Outline each Plasmodium falciparum-infected red blood cell.
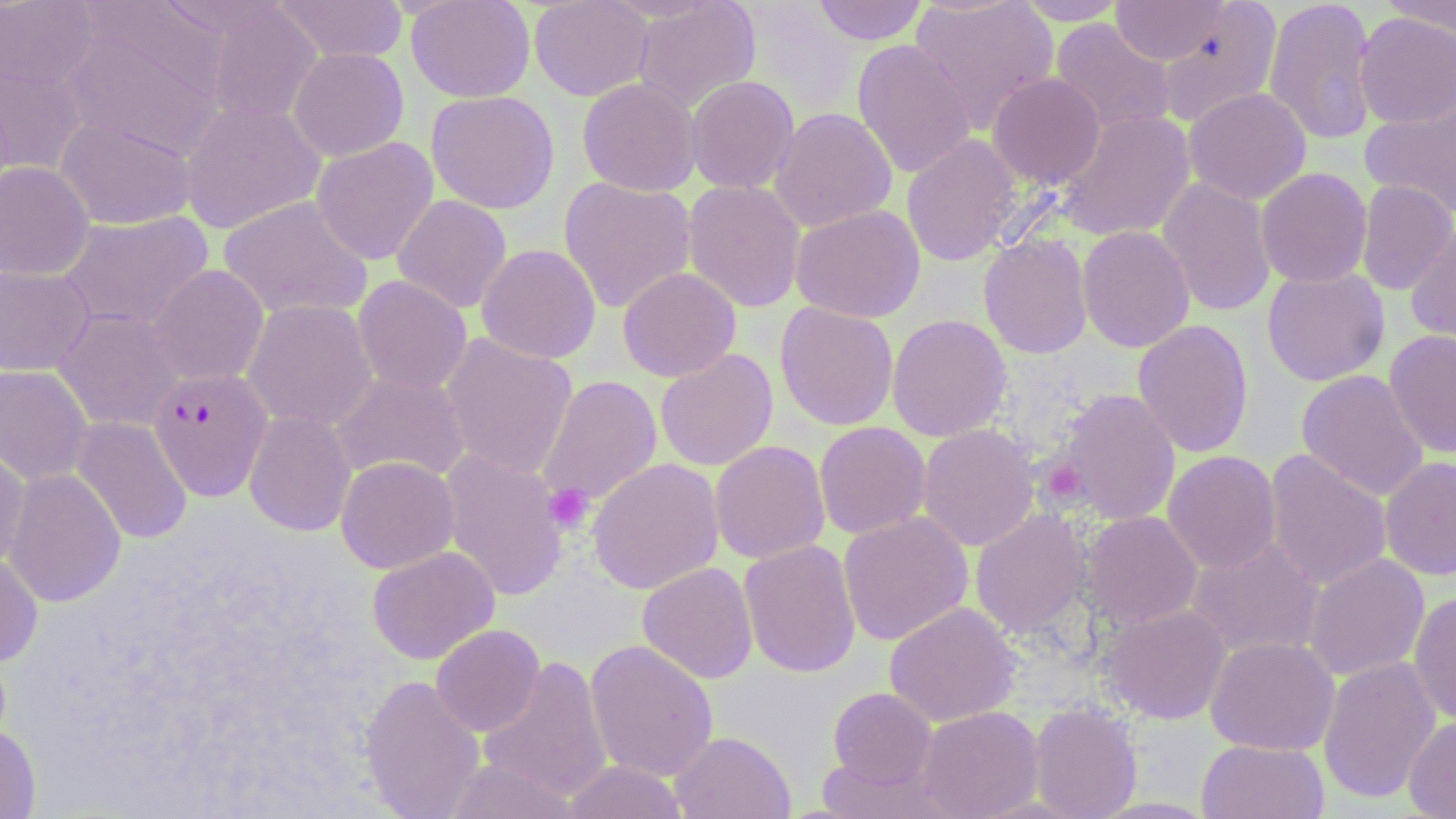
Approximate bounding boxes as (x1, y1, x2, y2) in pixels.
Plasmodium falciparum-infected red blood cells: (149, 367, 272, 501).

Uninfected red blood cell locations: (272, 0, 408, 64), (405, 0, 535, 102), (529, 0, 654, 101), (632, 0, 761, 113), (812, 0, 928, 45), (910, 0, 1058, 130), (1012, 0, 1130, 25), (1111, 0, 1228, 65), (1263, 0, 1378, 145), (0, 1, 98, 89), (1157, 1, 1283, 127), (1382, 1, 1456, 45), (206, 4, 323, 126), (61, 11, 227, 160), (1354, 11, 1456, 128), (1049, 18, 1176, 135), (852, 39, 977, 178), (288, 46, 409, 161), (0, 59, 89, 177), (987, 72, 1105, 189), (686, 76, 799, 195), (577, 77, 702, 197), (1184, 87, 1311, 204), (426, 90, 560, 214), (1360, 97, 1456, 220), (180, 99, 326, 234), (769, 107, 897, 232), (1056, 110, 1196, 241), (55, 115, 196, 230), (901, 133, 1021, 266), (311, 137, 439, 265), (0, 161, 94, 281), (1256, 167, 1373, 288), (558, 176, 697, 313), (1157, 177, 1277, 317), (683, 179, 806, 313), (1355, 180, 1455, 295), (392, 194, 512, 314), (218, 195, 373, 321), (791, 204, 925, 323), (57, 210, 214, 332), (1405, 221, 1456, 351), (1077, 225, 1195, 353), (978, 232, 1093, 360), (476, 243, 601, 364), (0, 264, 95, 376), (148, 264, 269, 386), (617, 267, 742, 382), (1262, 267, 1389, 386), (353, 275, 472, 394), (241, 299, 377, 432), (775, 302, 899, 431), (53, 307, 185, 433), (886, 314, 1013, 441), (1133, 318, 1254, 459), (1384, 329, 1456, 458), (440, 333, 578, 480), (655, 349, 778, 471), (0, 364, 93, 485), (1296, 369, 1429, 502), (330, 371, 470, 484), (537, 375, 662, 506), (1054, 388, 1181, 525), (244, 410, 356, 537), (71, 417, 192, 545), (814, 421, 931, 539), (917, 424, 1040, 551), (709, 440, 830, 564), (0, 444, 31, 569), (438, 448, 569, 601), (1263, 448, 1393, 592), (1162, 450, 1281, 573), (336, 456, 459, 574), (587, 457, 724, 594), (1379, 457, 1456, 580), (3, 468, 126, 608), (970, 509, 1092, 640), (1079, 511, 1203, 629), (838, 512, 973, 645), (1185, 536, 1325, 661), (738, 539, 862, 679), (367, 546, 499, 664), (0, 552, 43, 667), (1303, 553, 1430, 681), (637, 562, 758, 684), (1408, 591, 1456, 727), (884, 602, 1022, 726), (1099, 604, 1231, 724), (431, 624, 544, 736), (1205, 636, 1339, 756), (584, 639, 719, 782), (477, 655, 613, 804), (1317, 656, 1441, 804), (359, 674, 485, 819), (827, 687, 937, 789), (1030, 703, 1142, 819), (916, 706, 1043, 819), (1404, 716, 1456, 818), (0, 724, 41, 818), (670, 731, 796, 819), (1196, 739, 1329, 819), (443, 756, 578, 819), (560, 760, 690, 819). Platelet locations: (1041, 457, 1088, 506), (543, 484, 595, 535). Slide-level diagnosis: Plasmodium falciparum. May-Grünwald-Giemsa stain. Optical microscopy. Image is 1456×819 pixels. 1000x magnification. Thin blood smear. One field of a larger specimen.